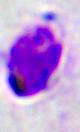

identification: leukocyte
modality: photomicrograph
magnification: 400x